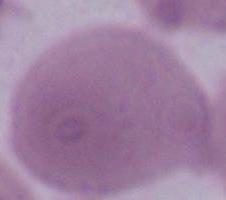

Summary:
  - Modality: photomicrograph
  - Magnification: 1000x
  - Identification: erythrocyte